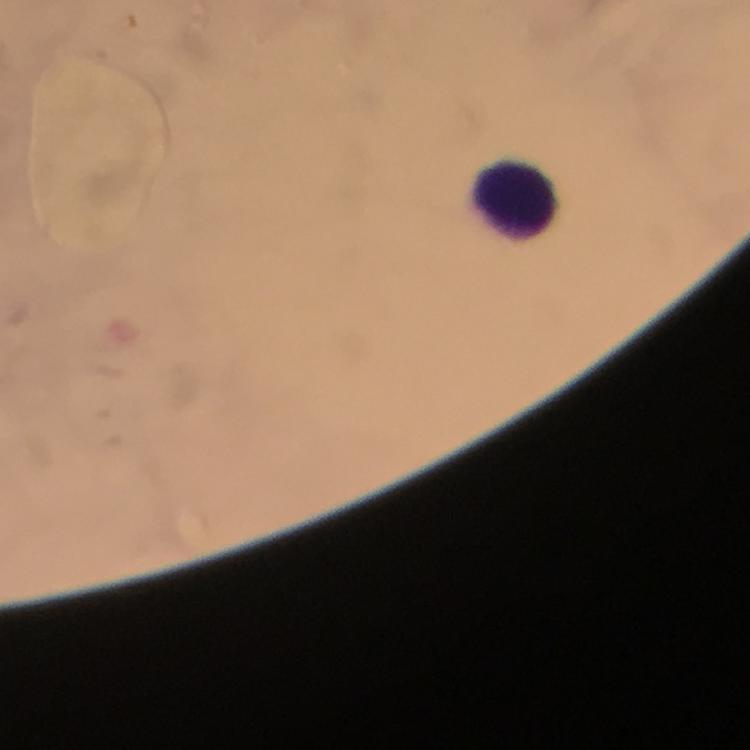 Approximate object centers, in pixels from the top-left corner. Leukocyte locations: (x=517, y=201). Giemsa-stained preparation. Plasmodium parasites: none detected. At 100x magnification. From a diagnostic examination for malaria. Thick smear. Image is 750×750 pixels. Photographed through the microscope with a smartphone camera. Immersion oil was used. A crop from one field of view.